Describe the morphology of the erythrocytes.
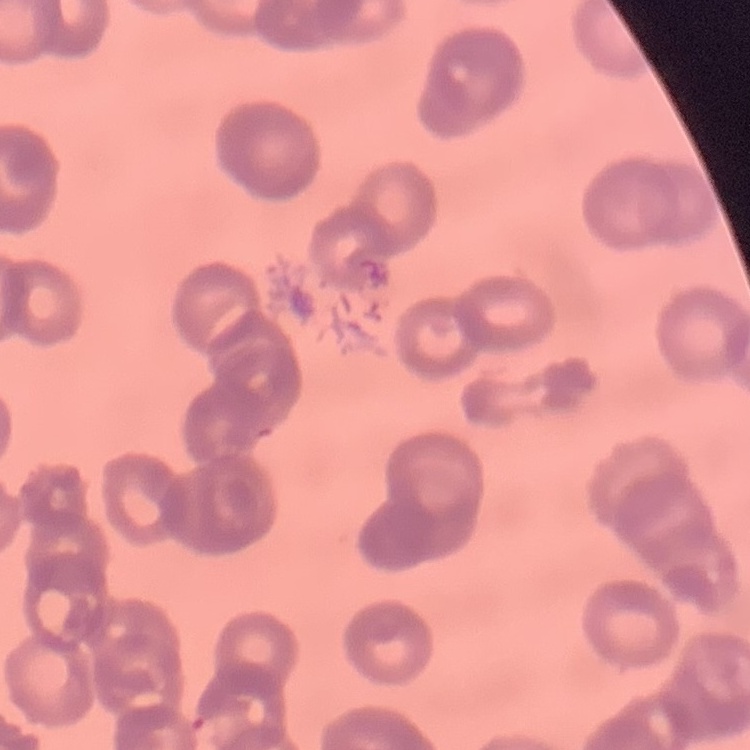
They show rouleaux formation.

Summary:
  - Preparation: thin peripheral smear
  - Stain: Field's or Giemsa
  - Image type: square crop of a larger photomicrograph